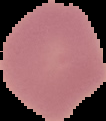
Summary:
  - Image type: segmented cell region on a black background
  - Result: no malaria parasites detected
  - Image size: 106×121 pixels
  - Preparation: thin blood film